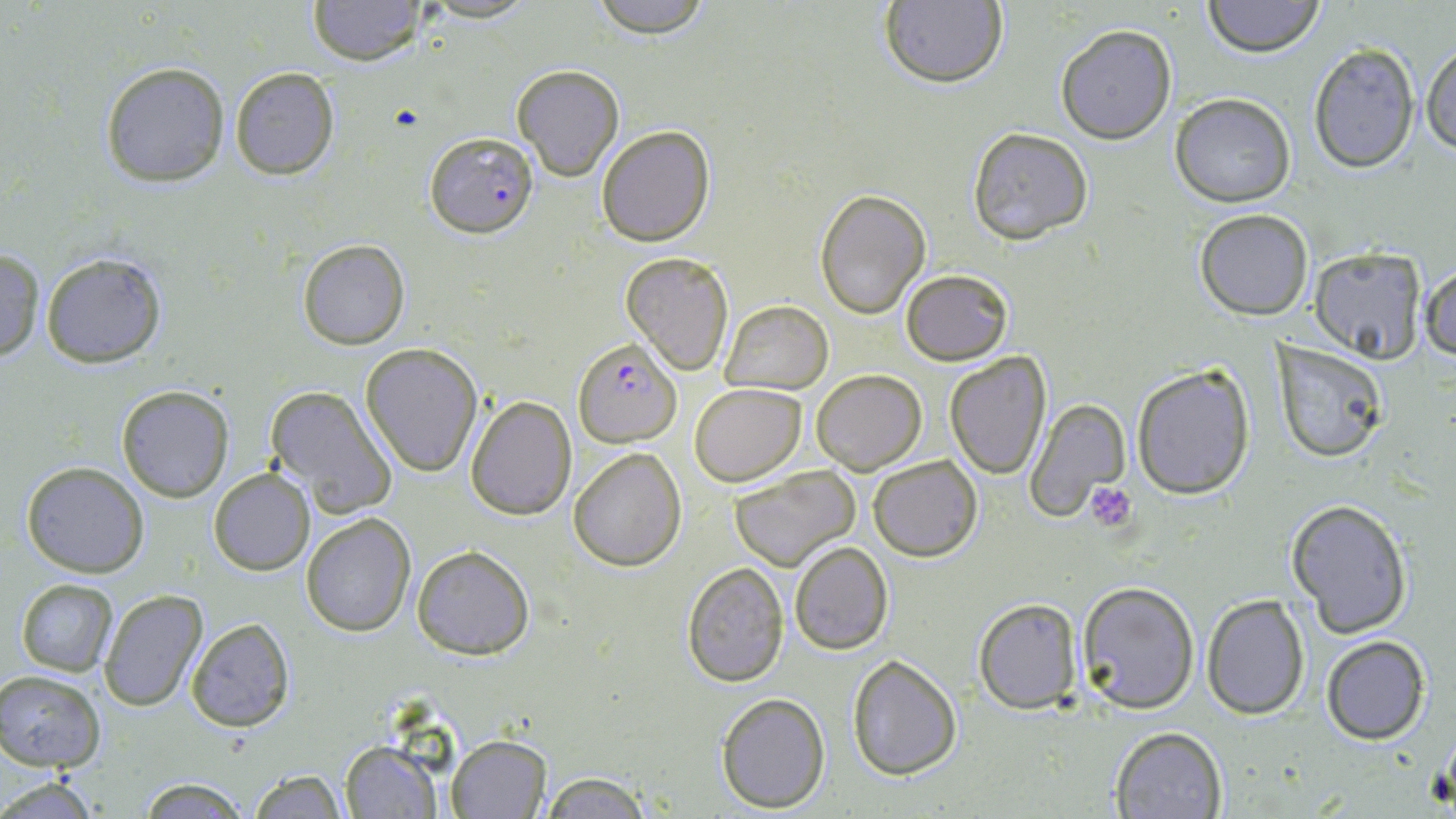

Summary:
  - Coordinate format: approximate bounding boxes as (x1, y1, x2, y2) in pixels
  - Uninfected red blood cell locations: (308, 0, 427, 65), (417, 0, 539, 23), (586, 0, 715, 35), (1204, 0, 1325, 57), (879, 1, 1007, 89), (1055, 24, 1177, 145), (1420, 38, 1455, 157), (1307, 42, 1419, 174), (99, 61, 229, 187), (511, 64, 624, 180), (229, 67, 339, 180), (1170, 93, 1295, 207), (595, 125, 715, 247), (966, 128, 1093, 243), (815, 188, 929, 321), (1193, 208, 1314, 319), (296, 238, 410, 350), (1309, 246, 1428, 362), (40, 249, 168, 368), (0, 250, 46, 361), (621, 252, 734, 375), (1420, 260, 1455, 365), (900, 268, 1014, 365), (720, 300, 832, 395), (1271, 341, 1392, 462), (361, 344, 482, 477), (944, 351, 1052, 479), (1131, 364, 1257, 500), (811, 368, 927, 474), (689, 383, 807, 486), (264, 384, 398, 518), (116, 385, 233, 502), (465, 395, 576, 520), (1025, 399, 1129, 522), (568, 448, 686, 571), (868, 454, 982, 562), (21, 461, 150, 578), (729, 464, 859, 570), (208, 468, 315, 577), (1285, 496, 1414, 640), (301, 513, 415, 637), (789, 541, 894, 656), (411, 545, 535, 659), (681, 562, 791, 685), (15, 578, 119, 675), (1076, 581, 1201, 715), (99, 590, 207, 712), (1201, 593, 1311, 720), (972, 598, 1083, 713), (185, 617, 297, 732), (1321, 636, 1430, 746), (846, 652, 963, 778), (0, 671, 106, 772), (716, 691, 830, 810), (1111, 726, 1227, 819), (445, 734, 555, 818), (338, 741, 441, 817), (248, 769, 351, 818), (540, 771, 651, 817), (0, 774, 105, 818), (137, 777, 250, 816)
  - Plasmodium falciparum-infected red blood cell locations: (426, 132, 537, 236), (577, 338, 685, 447)
  - Platelet locations: (1084, 482, 1137, 530)
  - Slide-level diagnosis: Plasmodium falciparum
  - Preparation: thin blood smear
  - Stain: May-Grünwald-Giemsa
  - Modality: light microscopy
  - Magnification: 1000x
  - Image size: 1456×819 pixels
  - Field of view: one of a larger specimen